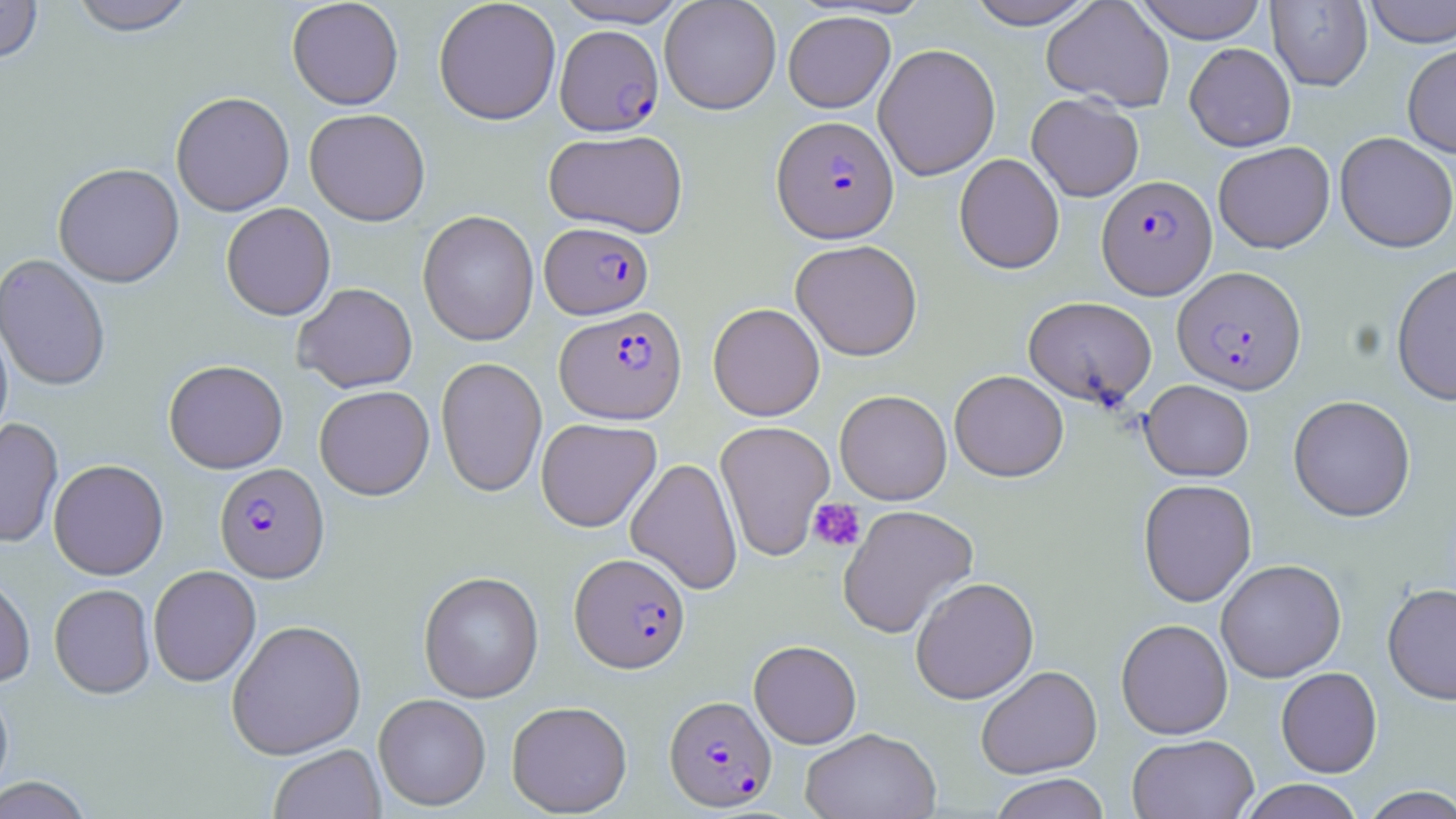
Summary:
  - Coordinate format: approximate bounding boxes as (x1, y1, x2, y2) in pixels
  - Plasmodium falciparum-infected red blood cell locations: (555, 25, 664, 136), (771, 115, 899, 243), (1097, 175, 1217, 299), (540, 222, 654, 319), (1172, 266, 1307, 394), (555, 306, 687, 424), (214, 463, 330, 582), (570, 552, 690, 673), (664, 695, 776, 811)
  - Uninfected red blood cell locations: (0, 0, 44, 65), (67, 0, 197, 36), (286, 0, 404, 110), (433, 0, 562, 125), (553, 0, 692, 27), (964, 0, 1099, 29), (1041, 0, 1174, 112), (1133, 0, 1268, 43), (1362, 0, 1456, 48), (659, 1, 782, 114), (1266, 1, 1373, 91), (783, 10, 896, 113), (1184, 42, 1296, 151), (873, 43, 1000, 181), (1402, 43, 1456, 158), (170, 91, 295, 216), (1026, 93, 1144, 202), (305, 108, 430, 226), (543, 129, 688, 238), (1334, 132, 1456, 253), (1213, 141, 1335, 253), (954, 153, 1065, 274), (52, 163, 184, 287), (221, 202, 336, 321), (418, 210, 539, 346), (790, 239, 923, 361), (0, 254, 111, 392), (1391, 262, 1456, 405), (292, 283, 418, 393), (1023, 296, 1156, 406), (708, 302, 825, 421), (0, 317, 13, 446), (435, 356, 547, 497), (163, 359, 288, 473), (949, 370, 1068, 481), (1140, 380, 1254, 481), (314, 385, 434, 500), (834, 389, 953, 505), (1288, 394, 1416, 522), (0, 418, 63, 548), (535, 418, 661, 532), (715, 420, 835, 560), (626, 457, 742, 594), (48, 459, 169, 580), (1138, 478, 1257, 607), (837, 504, 979, 639), (1216, 558, 1346, 682), (148, 565, 261, 686), (418, 571, 544, 702), (0, 572, 36, 688), (910, 576, 1039, 704), (49, 583, 155, 699), (1382, 583, 1456, 704), (226, 618, 366, 759), (1116, 618, 1233, 739), (749, 640, 862, 748), (975, 665, 1102, 779), (1276, 666, 1382, 778), (0, 682, 14, 800), (373, 693, 491, 811), (506, 700, 633, 816), (800, 727, 941, 819), (1127, 734, 1260, 819), (268, 744, 386, 819), (989, 773, 1111, 819), (0, 776, 94, 819), (1238, 779, 1366, 819), (1359, 785, 1456, 819)
  - Platelet locations: (808, 498, 865, 552)
  - Slide-level diagnosis: Plasmodium falciparum
  - Image size: 1456×819 pixels
  - Modality: optical microscopy
  - Stain: May-Grünwald-Giemsa
  - Field of view: one of a larger specimen
  - Preparation: thin blood smear
  - Magnification: 1000x